Identify the cell.
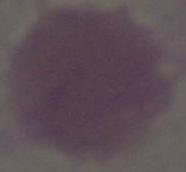

This is an erythrocyte.

modality = micrograph
magnification = 1000x